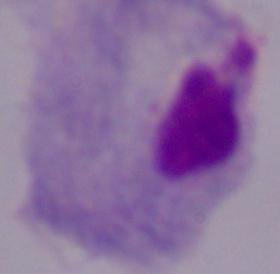

A trichomonad is seen. Photomicrograph. 1000x magnification.